Classify this cell by malaria status.
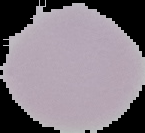
Uninfected.

From a thin blood smear. Segmented cell region on a black background. Image is 145×133 pixels.